Outline every malaria parasite.
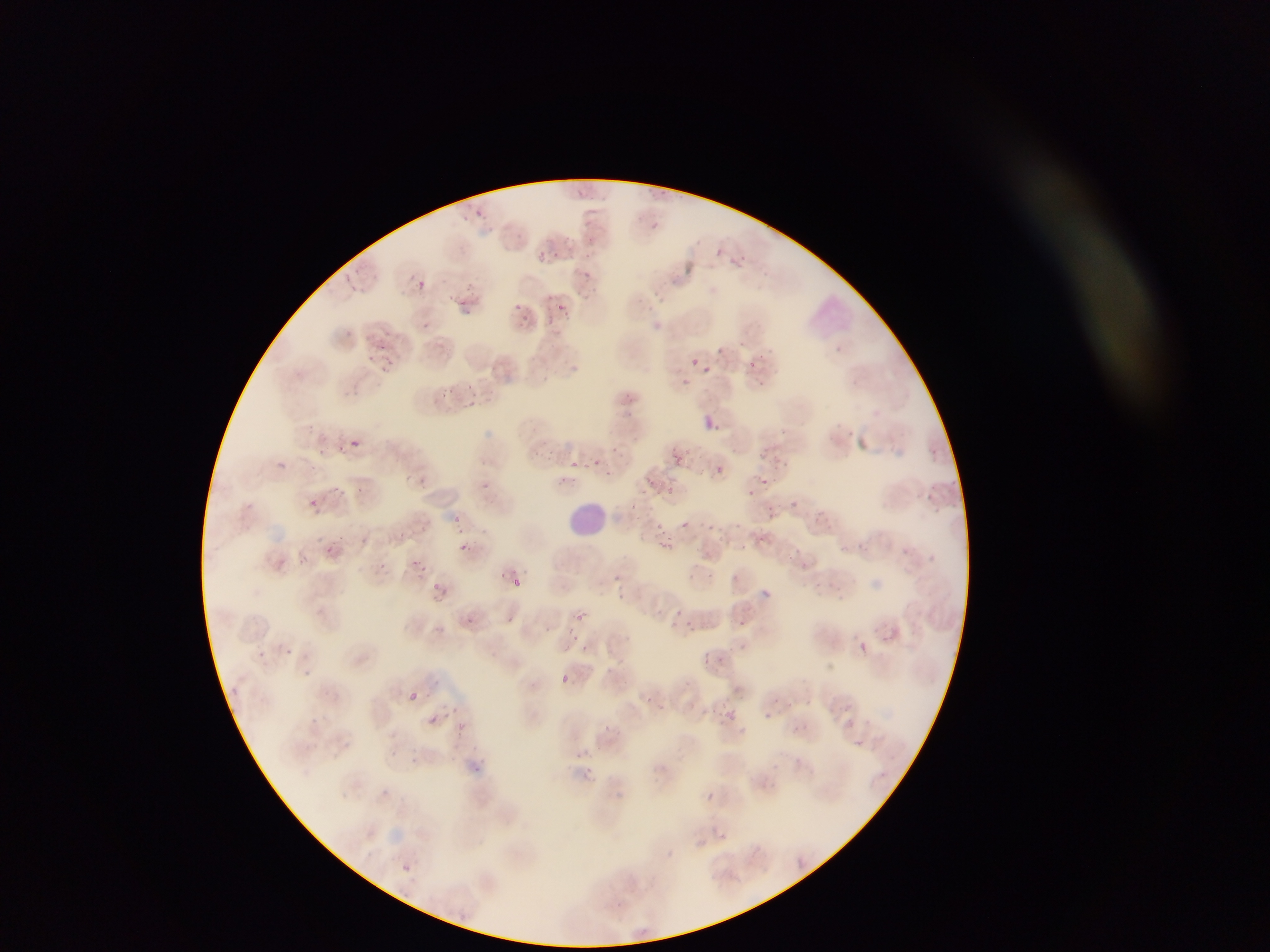
Approximate bounding boxes as {left, top, right, bottom} in pixels.
Malaria parasites: {645, 185, 656, 196}, {575, 186, 587, 198}, {658, 189, 677, 197}, {463, 202, 474, 209}, {462, 211, 471, 230}, {477, 212, 495, 223}, {583, 214, 596, 227}, {651, 219, 660, 232}, {586, 232, 596, 246}, {564, 234, 575, 246}, {712, 245, 723, 259}, {534, 250, 555, 265}, {742, 251, 751, 264}, {351, 265, 364, 280}, {583, 269, 592, 280}, {344, 276, 354, 283}, {417, 280, 427, 290}, {466, 280, 479, 294}, {652, 287, 668, 305}, {547, 293, 554, 302}, {455, 298, 465, 308}, {513, 301, 521, 309}, {558, 304, 568, 314}, {520, 314, 531, 325}, {547, 314, 555, 326}, {420, 321, 433, 337}, {345, 328, 354, 335}, {376, 343, 387, 351}, {834, 344, 844, 353}, {716, 346, 725, 356}, {763, 348, 778, 359}, {385, 353, 399, 370}, {691, 357, 701, 366}, {748, 359, 762, 372}, {703, 364, 712, 372}, {681, 378, 691, 387}, {464, 384, 474, 390}, {443, 386, 457, 397}, {470, 399, 480, 410}, {705, 416, 718, 429}, {351, 438, 360, 446}, {340, 443, 347, 454}, {611, 443, 622, 457}, {667, 445, 685, 460}, {318, 448, 330, 457}, {763, 453, 769, 461}, {585, 457, 591, 473}, {596, 459, 604, 468}, {277, 460, 285, 468}, {568, 460, 578, 474}, {773, 461, 785, 471}, {714, 464, 723, 475}, {604, 468, 622, 476}, {403, 470, 413, 482}, {762, 474, 770, 486}, {414, 475, 427, 493}, {559, 476, 566, 487}, {647, 476, 656, 490}, {927, 480, 942, 491}, {666, 481, 680, 497}, {480, 483, 494, 492}, {355, 484, 365, 496}, {333, 485, 342, 493}, {749, 487, 759, 500}, {794, 497, 804, 509}, {309, 499, 318, 507}, {632, 499, 641, 510}, {767, 505, 779, 526}, {818, 505, 835, 523}, {452, 514, 464, 526}, {655, 520, 669, 535}, {671, 521, 688, 533}, {709, 523, 715, 532}, {331, 538, 338, 546}, {360, 538, 368, 547}, {856, 538, 867, 556}, {657, 540, 672, 556}, {461, 543, 470, 551}, {741, 543, 749, 553}, {324, 548, 332, 556}, {842, 548, 854, 558}, {295, 555, 306, 564}, {278, 557, 286, 563}, {414, 558, 425, 567}, {799, 559, 809, 571}, {511, 565, 519, 577}, {497, 570, 510, 586}, {613, 573, 622, 582}, {513, 578, 521, 587}, {432, 582, 442, 591}, {571, 614, 583, 620}, {463, 616, 474, 626}, {507, 616, 517, 626}, {672, 620, 682, 632}, {738, 620, 749, 631}, {682, 621, 695, 627}, {570, 633, 582, 642}, {859, 643, 867, 651}, {579, 644, 590, 654}, {284, 647, 292, 654}, {702, 652, 713, 667}, {721, 655, 729, 668}, {561, 675, 569, 683}, {409, 693, 417, 700}, {722, 703, 745, 726}, {452, 706, 459, 714}, {763, 713, 772, 721}, {428, 716, 439, 726}, {604, 723, 612, 731}, {769, 761, 777, 770}, {879, 771, 887, 778}, {706, 792, 714, 801}, {720, 832, 729, 840}, {402, 863, 412, 873} | approximate {x, y} pixel centers of objects too small to bound: {371, 359}, {820, 584}, {678, 612}, {307, 673}.

Leukocyte locations: {567, 500, 604, 539}. Sample from Ghana. Photographed through a microscope with a mobile-phone camera. Single field of view. Thin blood film. Image is 1270×952 pixels.